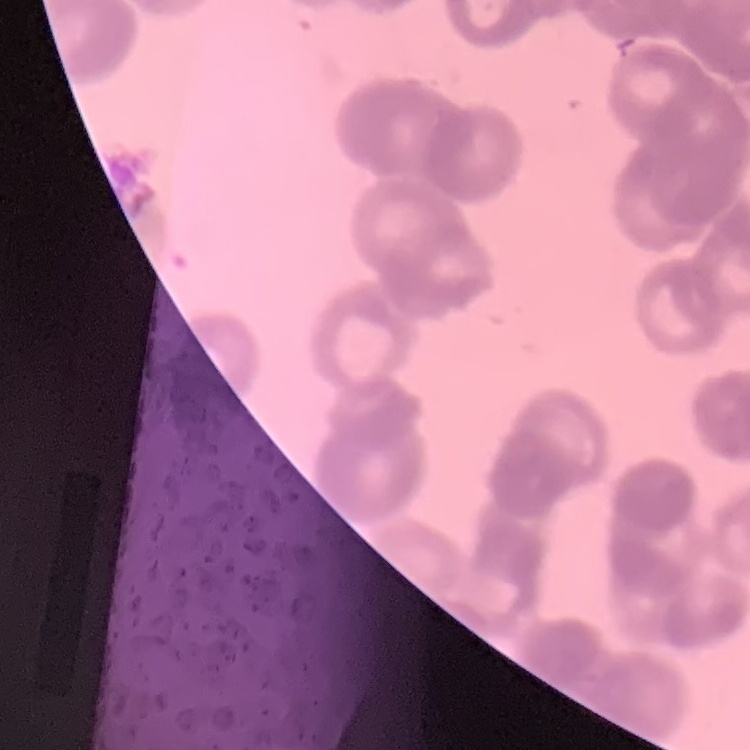
erythrocyte morphology = rouleaux formation
preparation = thin blood smear
stain = Field's or Giemsa
image type = one tile cut from a larger photomicrograph